Name the blood parasite species.
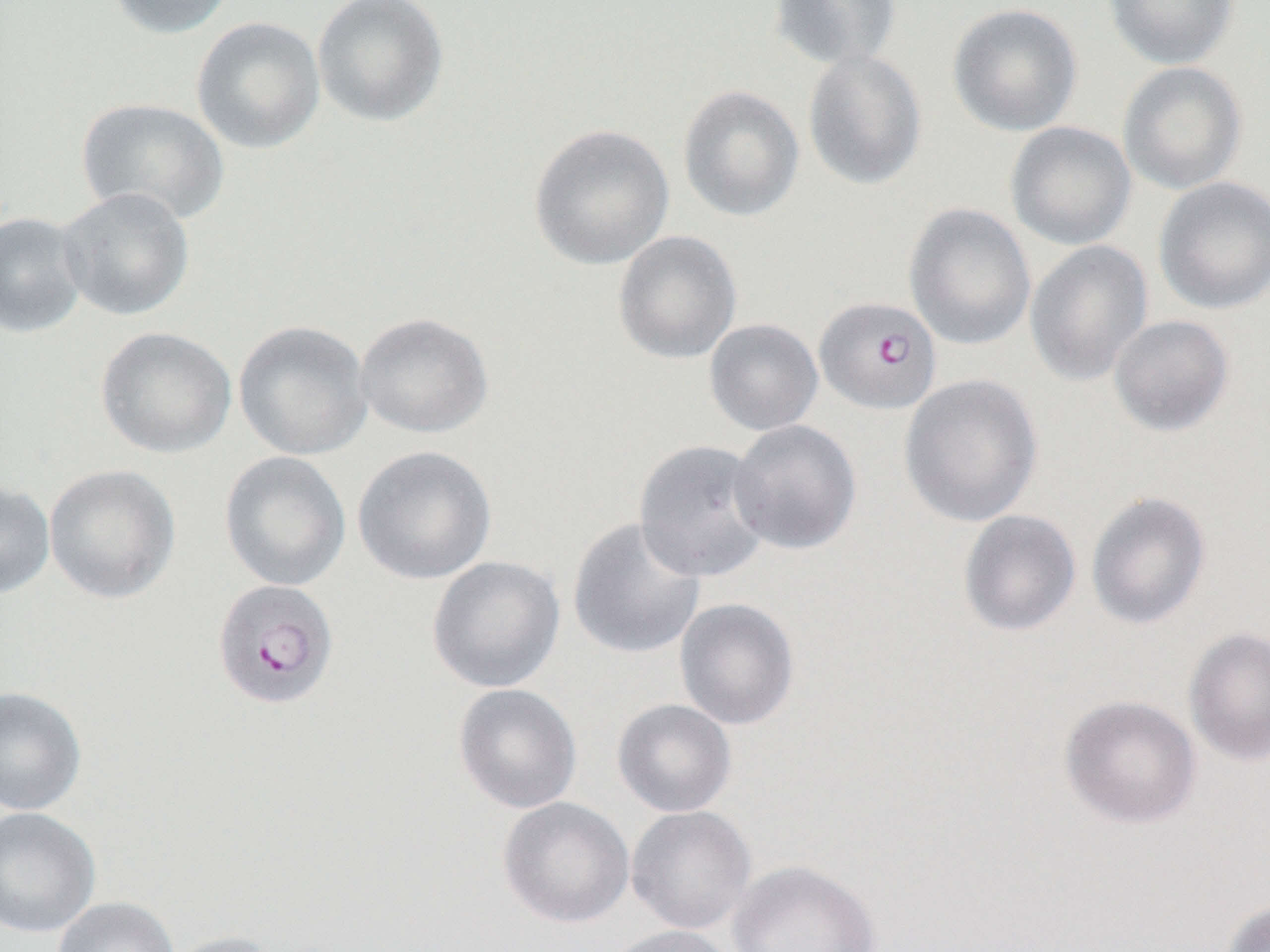

Plasmodium falciparum.

Approximate bounding boxes as [x1, y1, x2, y2] in pixels. Plasmodium falciparum-infected red blood cell locations: [814, 296, 942, 414], [212, 578, 339, 711]. Uninfected red blood cell locations: [104, 0, 237, 39], [312, 0, 448, 127], [769, 0, 903, 71], [1103, 0, 1239, 70], [947, 3, 1083, 137], [191, 16, 326, 154], [803, 48, 927, 192], [1118, 61, 1248, 195], [678, 85, 805, 223], [76, 96, 230, 226], [1005, 121, 1137, 250], [528, 123, 675, 270], [1153, 176, 1270, 315], [56, 187, 195, 321], [904, 203, 1036, 351], [0, 211, 89, 337], [612, 230, 742, 365], [1025, 240, 1153, 387], [355, 313, 493, 439], [1108, 314, 1235, 437], [704, 318, 823, 436], [233, 320, 373, 460], [95, 326, 237, 458], [899, 373, 1043, 527], [728, 420, 862, 555], [633, 439, 772, 582], [352, 445, 497, 585], [219, 451, 351, 591], [43, 463, 181, 604], [0, 481, 55, 598], [1086, 491, 1211, 631], [958, 509, 1081, 636], [567, 517, 706, 660], [427, 555, 565, 693], [675, 598, 800, 730], [1184, 627, 1270, 767], [453, 684, 582, 814], [0, 686, 87, 816], [1060, 695, 1201, 828], [613, 698, 737, 817], [498, 796, 635, 928], [626, 805, 756, 935], [0, 807, 101, 938], [727, 859, 881, 952], [52, 896, 180, 952], [1221, 899, 1270, 952], [605, 925, 739, 952], [157, 930, 285, 952]. Image is 1270×952 pixels. Captured at 1000x magnification. Light microscopy. Thin blood smear. Single field of view.